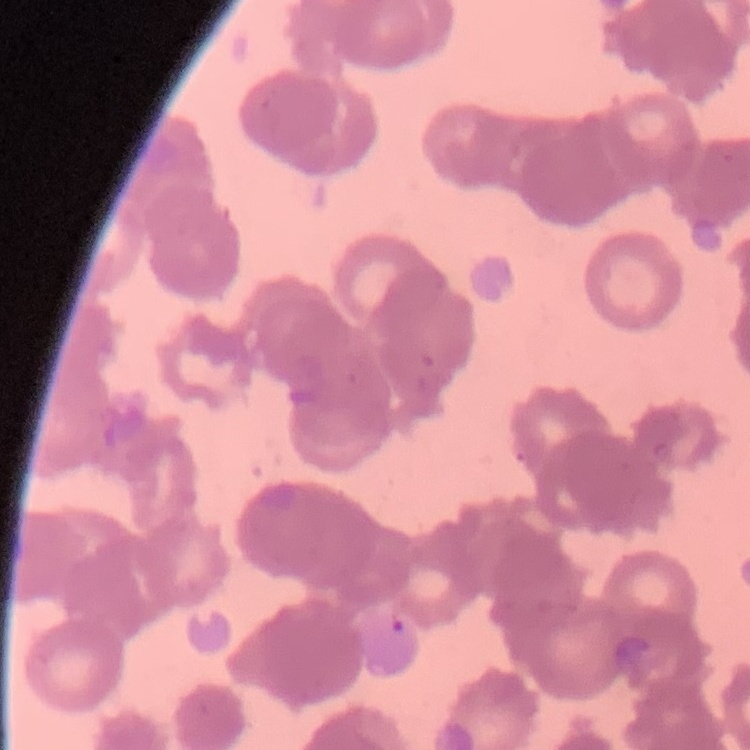

Summary:
  - Erythrocyte morphology: rouleaux formation
  - Preparation: thin blood film
  - Stain: Field's or Giemsa
  - Image type: one tile cut from a larger photomicrograph